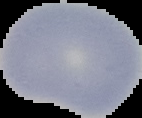

Image is 142×118 pixels. From a thin blood smear. The area outside the segmented cell region is set to black. Result: no malaria parasites seen.